Report the malaria status of this cell.
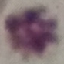

Uninfected.

Summary:
  - Stain: Giemsa
  - Preparation: thin blood smear
  - Capture: smartphone camera at the microscope eyepiece
  - Image type: automatically extracted cell patch, resized to 64 × 64 pixels